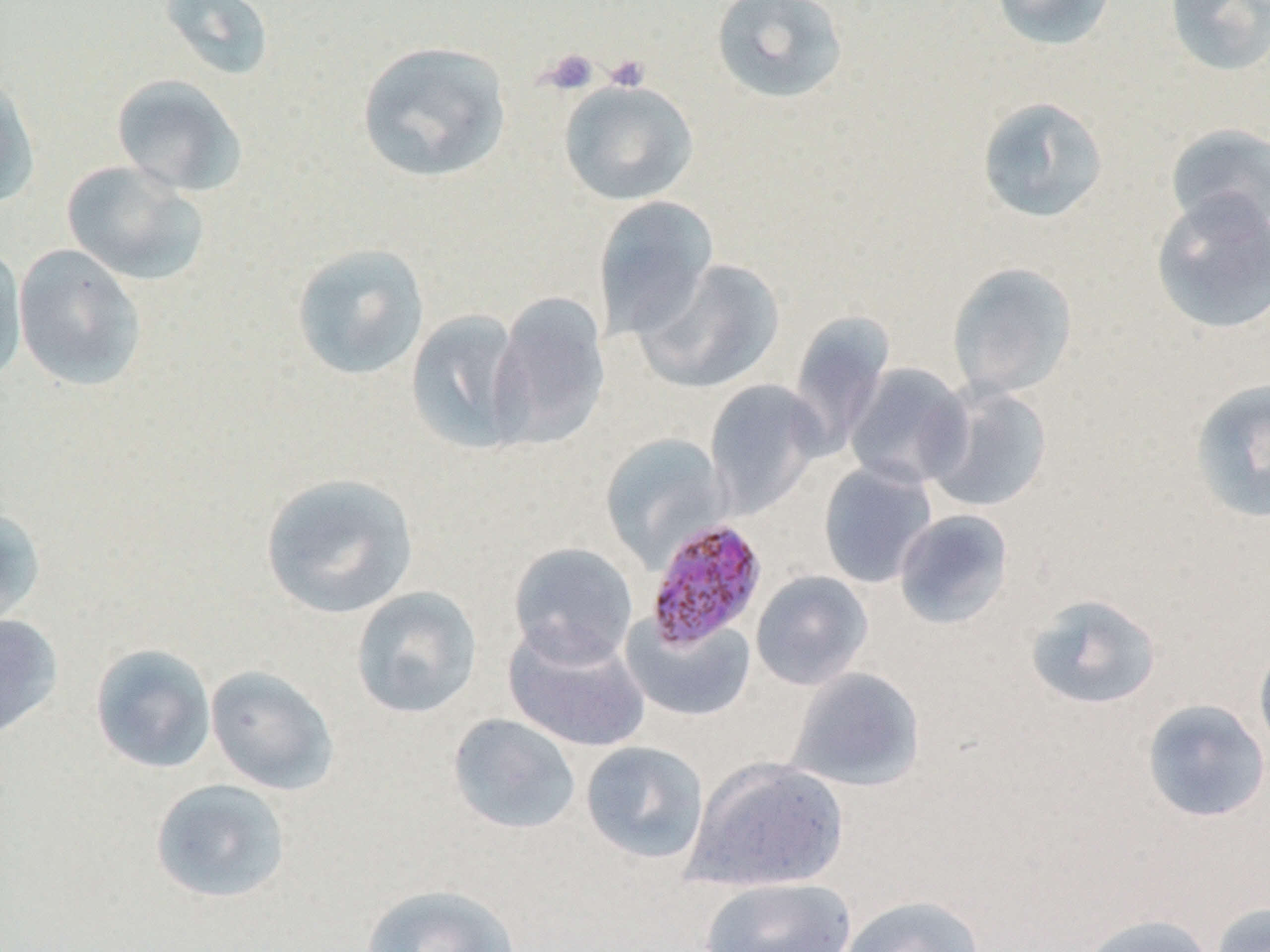 Approximate bounding boxes as (x1, y1, x2, y2) in pixels. Plasmodium malariae-infected red blood cell locations: (644, 517, 769, 652). Platelet locations: (539, 48, 599, 96), (604, 54, 651, 92). Uninfected red blood cell locations: (159, 0, 276, 81), (711, 0, 850, 106), (990, 0, 1118, 51), (1165, 0, 1270, 77), (357, 39, 513, 183), (0, 71, 40, 209), (111, 74, 248, 197), (558, 78, 699, 206), (977, 96, 1109, 223), (1165, 123, 1269, 238), (61, 160, 209, 287), (1150, 191, 1270, 335), (593, 195, 719, 341), (291, 242, 430, 381), (13, 244, 148, 392), (0, 248, 28, 386), (634, 259, 787, 393), (947, 262, 1078, 399), (489, 292, 609, 449), (405, 309, 530, 454), (788, 311, 894, 453), (843, 363, 974, 491), (1188, 377, 1270, 524), (704, 379, 826, 518), (924, 382, 1053, 513), (599, 432, 727, 569), (817, 461, 937, 588), (259, 471, 419, 619), (0, 506, 47, 631), (893, 509, 1014, 630), (508, 543, 639, 666), (751, 570, 873, 691), (351, 586, 483, 719), (1024, 593, 1163, 711), (621, 612, 756, 722), (0, 614, 63, 739), (503, 622, 650, 753), (1254, 639, 1270, 763), (90, 644, 217, 774), (205, 664, 340, 796), (786, 667, 925, 792), (1141, 699, 1270, 823), (447, 713, 581, 834), (580, 741, 709, 864), (684, 755, 849, 893), (149, 778, 292, 904), (699, 876, 858, 952), (361, 883, 521, 952), (839, 894, 986, 952), (1210, 901, 1270, 952), (1076, 914, 1216, 952). Slide-level diagnosis: Plasmodium malariae. Thin blood film. One field of a larger specimen. Captured at 1000x magnification. Optical microscopy. Image is 1270×952 pixels.